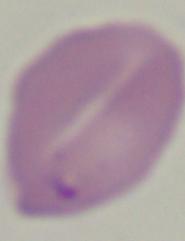

magnification = 1000x
modality = photomicrograph
identification = Babesia